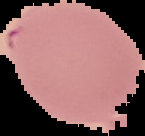
preparation: thin blood smear
image_type: segmented cell region with the area outside set to black
image_size: 145×136 pixels
malaria_status: parasitized